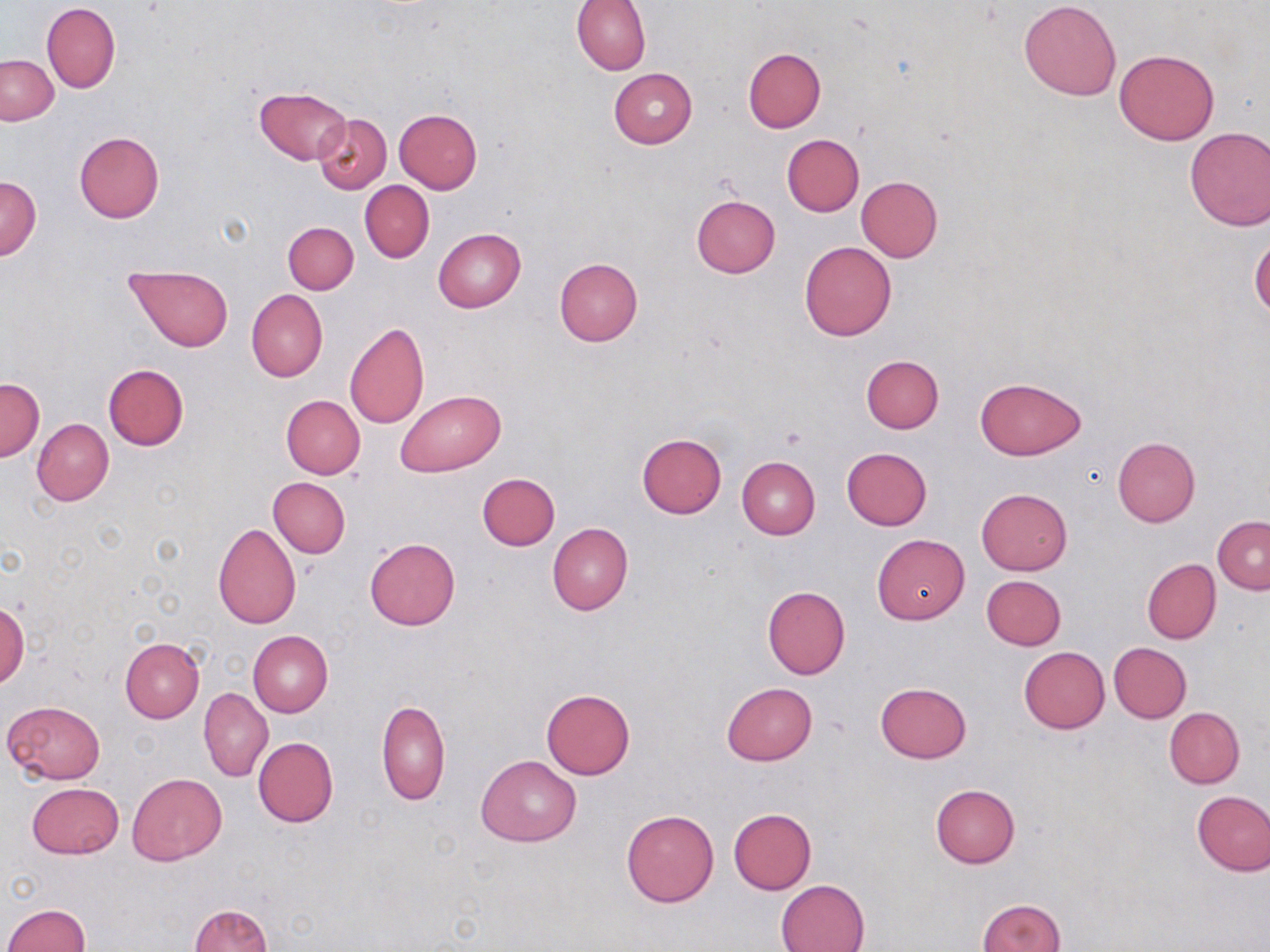

Approximate bounding boxes as named x1/y1/x2/y2 corners in pixels. Uninfected red blood cell locations: (x1=572, y1=0, x2=651, y2=75), (x1=1019, y1=0, x2=1122, y2=101), (x1=42, y1=2, x2=120, y2=93), (x1=742, y1=48, x2=826, y2=132), (x1=1115, y1=49, x2=1219, y2=145), (x1=1, y1=55, x2=58, y2=125), (x1=608, y1=68, x2=698, y2=148), (x1=254, y1=86, x2=352, y2=165), (x1=394, y1=108, x2=482, y2=193), (x1=312, y1=114, x2=391, y2=193), (x1=1183, y1=126, x2=1270, y2=231), (x1=74, y1=130, x2=165, y2=223), (x1=782, y1=135, x2=864, y2=216), (x1=855, y1=176, x2=943, y2=261), (x1=0, y1=177, x2=41, y2=259), (x1=360, y1=181, x2=434, y2=262), (x1=691, y1=194, x2=780, y2=278), (x1=283, y1=221, x2=358, y2=294), (x1=433, y1=228, x2=525, y2=312), (x1=1249, y1=236, x2=1270, y2=320), (x1=799, y1=241, x2=896, y2=341), (x1=554, y1=256, x2=643, y2=346), (x1=126, y1=265, x2=234, y2=352), (x1=246, y1=290, x2=327, y2=382), (x1=345, y1=322, x2=429, y2=429), (x1=861, y1=354, x2=944, y2=433), (x1=103, y1=364, x2=189, y2=451), (x1=0, y1=377, x2=43, y2=460), (x1=976, y1=377, x2=1085, y2=460), (x1=395, y1=390, x2=506, y2=476), (x1=280, y1=395, x2=366, y2=479), (x1=32, y1=418, x2=113, y2=505), (x1=637, y1=433, x2=727, y2=518), (x1=1113, y1=437, x2=1200, y2=527), (x1=842, y1=447, x2=932, y2=530), (x1=737, y1=457, x2=819, y2=539), (x1=477, y1=472, x2=560, y2=550), (x1=267, y1=477, x2=350, y2=558), (x1=976, y1=488, x2=1072, y2=575), (x1=1213, y1=516, x2=1270, y2=594), (x1=548, y1=522, x2=633, y2=615), (x1=213, y1=523, x2=302, y2=628), (x1=872, y1=533, x2=969, y2=625), (x1=365, y1=537, x2=460, y2=629), (x1=1142, y1=559, x2=1221, y2=643), (x1=981, y1=575, x2=1066, y2=650), (x1=762, y1=587, x2=850, y2=679), (x1=1, y1=602, x2=28, y2=688), (x1=248, y1=631, x2=332, y2=717), (x1=120, y1=637, x2=204, y2=722), (x1=1108, y1=642, x2=1191, y2=723), (x1=1018, y1=647, x2=1110, y2=734), (x1=721, y1=682, x2=818, y2=766), (x1=876, y1=683, x2=971, y2=763), (x1=198, y1=687, x2=273, y2=781), (x1=542, y1=688, x2=635, y2=780), (x1=377, y1=699, x2=450, y2=806), (x1=3, y1=700, x2=106, y2=784), (x1=1165, y1=707, x2=1244, y2=787), (x1=252, y1=737, x2=339, y2=827), (x1=477, y1=755, x2=581, y2=846), (x1=127, y1=773, x2=226, y2=866), (x1=28, y1=781, x2=123, y2=858), (x1=930, y1=784, x2=1020, y2=867), (x1=1192, y1=789, x2=1270, y2=876), (x1=621, y1=808, x2=719, y2=907), (x1=728, y1=808, x2=817, y2=894), (x1=775, y1=879, x2=869, y2=952), (x1=977, y1=899, x2=1066, y2=952), (x1=1, y1=904, x2=89, y2=952), (x1=189, y1=904, x2=272, y2=952). Platelet locations: (x1=778, y1=427, x2=806, y2=450). Slide-level diagnosis: no evidence of blood parasites. Light microscopy. Single field of view. May-Grünwald-Giemsa-stained preparation. Thin blood film. 1000x magnification. Image is 1270×952 pixels.